Name the parasite shown.
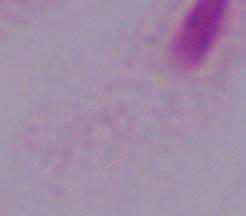
A trichomonad.

magnification = 1000x
modality = photomicrograph